Locate every uninfected red blood cell.
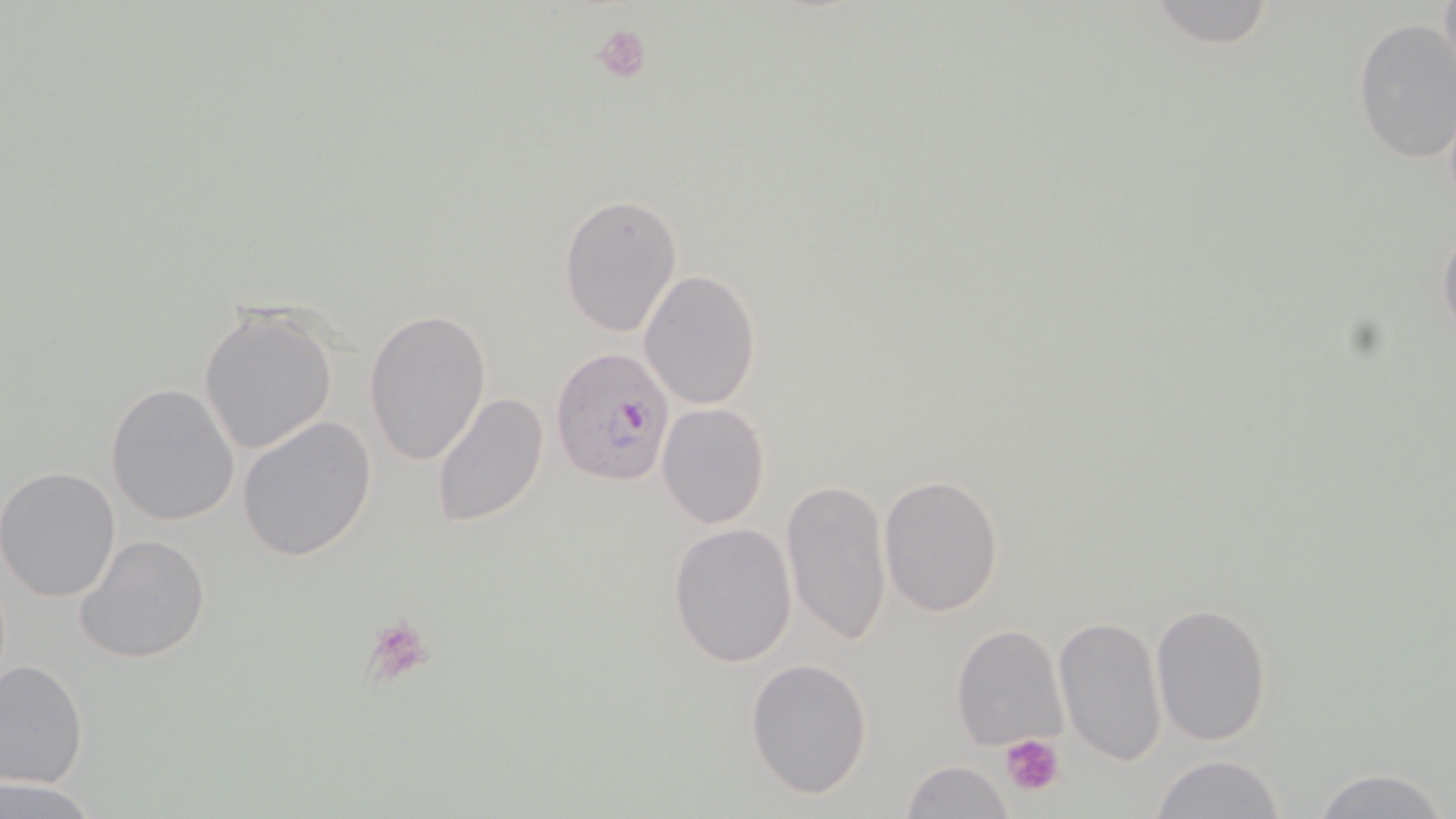
Approximate bounding boxes as (x1, y1, x2, y2) in pixels.
Uninfected red blood cells: (1146, 0, 1281, 49), (1353, 17, 1456, 165), (559, 195, 682, 336), (1438, 218, 1456, 347), (638, 270, 762, 410), (197, 306, 338, 456), (364, 309, 491, 465), (105, 382, 240, 527), (430, 391, 550, 530), (656, 402, 771, 529), (236, 415, 378, 562), (0, 467, 122, 601), (878, 474, 1004, 617), (781, 477, 891, 651), (667, 522, 799, 669), (74, 532, 211, 665), (1150, 602, 1274, 745), (1053, 614, 1169, 768), (951, 625, 1069, 750), (745, 655, 873, 798), (1, 659, 90, 789), (1152, 754, 1287, 819), (900, 760, 1017, 819), (1308, 766, 1449, 819), (1, 778, 99, 816).

Platelet locations: (591, 21, 654, 84), (360, 616, 437, 687), (1001, 733, 1065, 799). Plasmodium falciparum-infected red blood cell locations: (550, 346, 676, 488). Slide-level diagnosis: Plasmodium falciparum. Image is 1456×819 pixels. Single field of view. May-Grünwald-Giemsa-stained preparation. 1000x magnification. Light microscopy. Thin blood film.